Identify the preparation type.
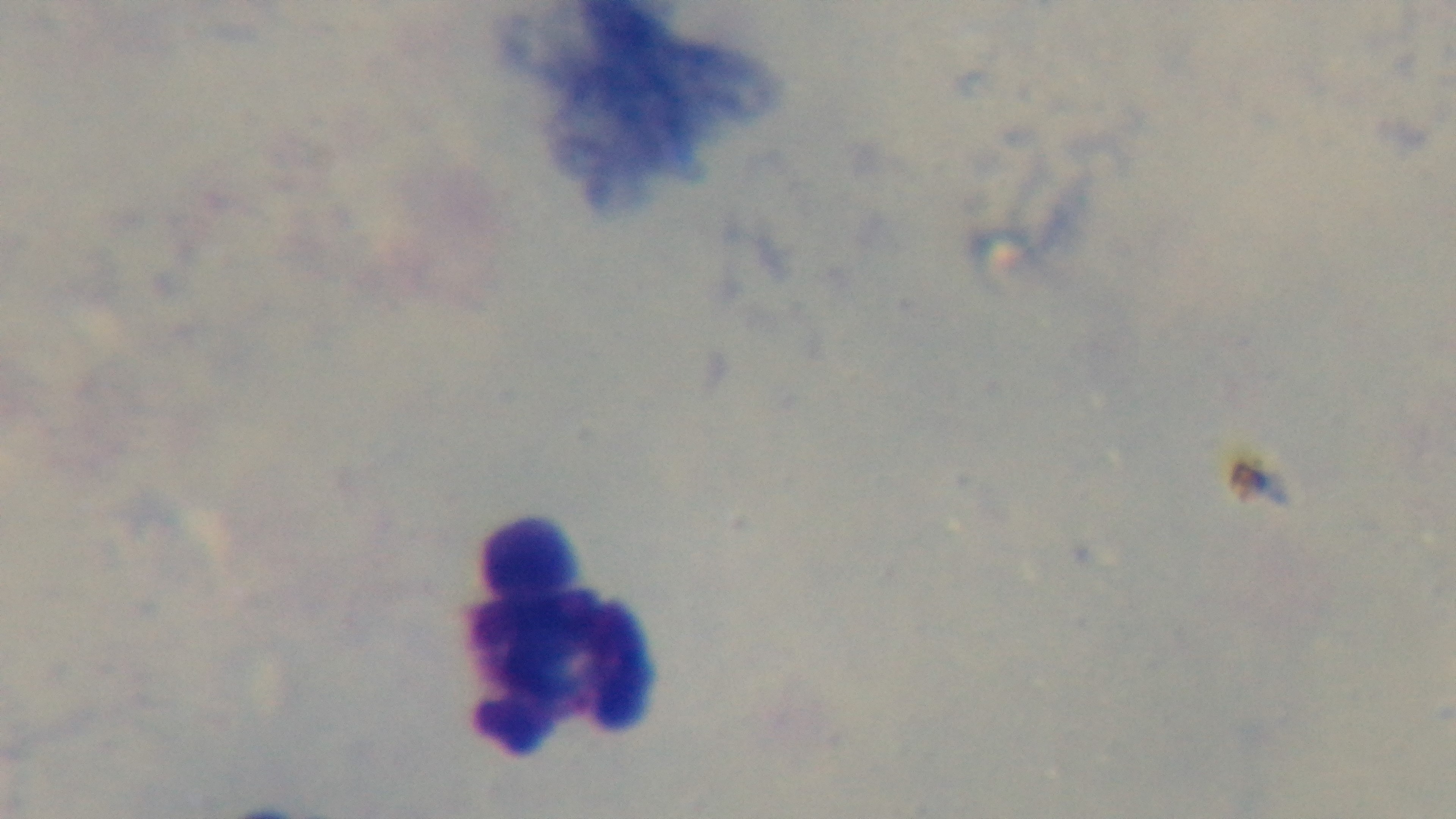

It is a thick blood film.

Light microscopy. 100x oil-immersion objective. Giemsa stain. Malaria status: negative. Mounted 4K digital camera. Single field of view.